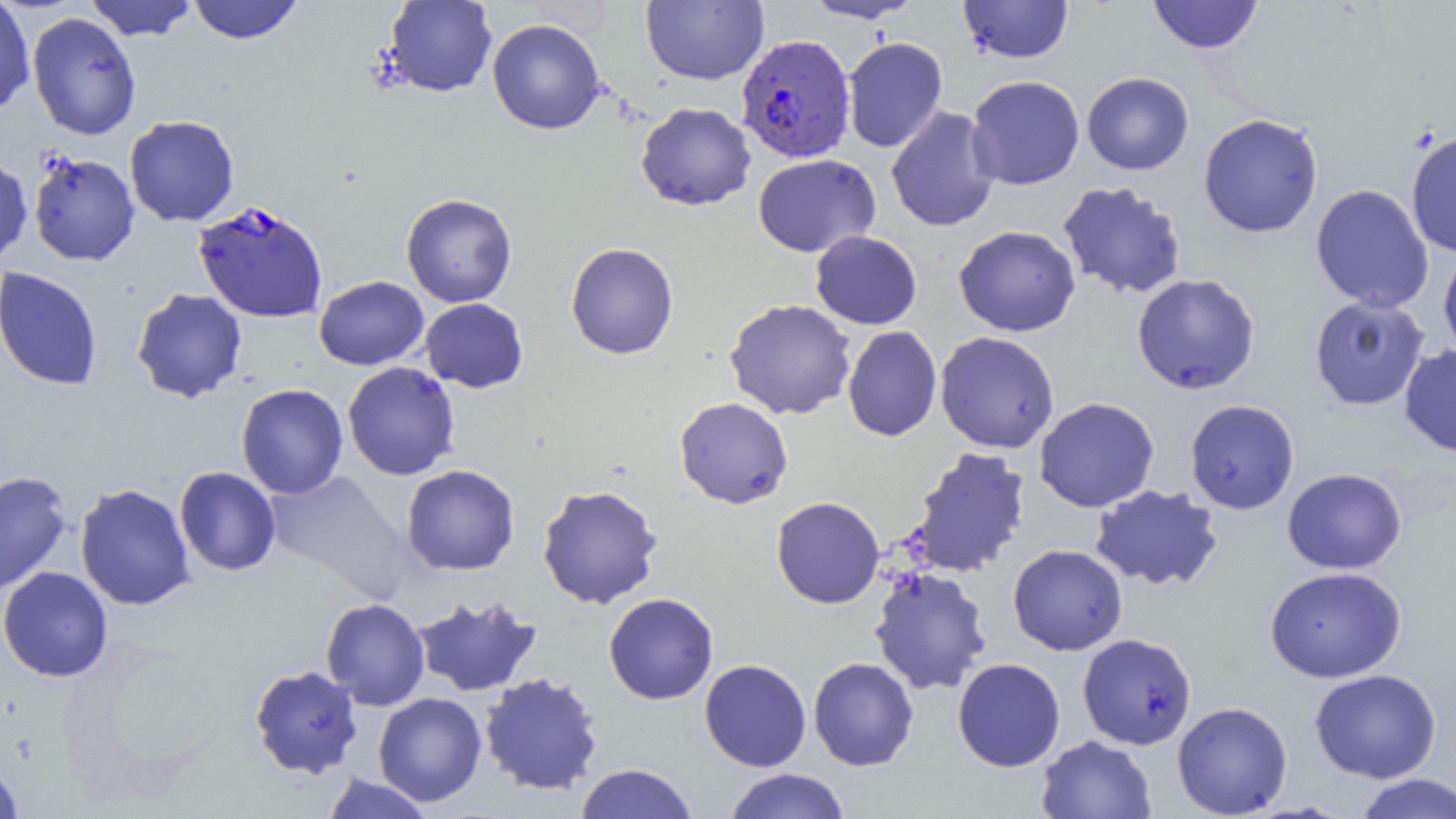

Approximate bounding boxes as named x1/y1/x2/y2 corners in pixels. Plasmodium falciparum-infected red blood cell locations: (x1=736, y1=34, x2=856, y2=163), (x1=193, y1=200, x2=328, y2=323). Uninfected red blood cell locations: (x1=0, y1=0, x2=35, y2=118), (x1=85, y1=0, x2=197, y2=41), (x1=187, y1=0, x2=304, y2=44), (x1=640, y1=0, x2=768, y2=85), (x1=802, y1=0, x2=923, y2=23), (x1=958, y1=0, x2=1074, y2=64), (x1=1147, y1=0, x2=1264, y2=54), (x1=382, y1=1, x2=498, y2=97), (x1=27, y1=11, x2=141, y2=140), (x1=487, y1=18, x2=605, y2=134), (x1=842, y1=37, x2=948, y2=153), (x1=1082, y1=72, x2=1194, y2=175), (x1=966, y1=75, x2=1084, y2=190), (x1=636, y1=101, x2=756, y2=211), (x1=886, y1=105, x2=1000, y2=232), (x1=1198, y1=113, x2=1324, y2=238), (x1=124, y1=115, x2=240, y2=227), (x1=1406, y1=130, x2=1456, y2=257), (x1=28, y1=151, x2=140, y2=266), (x1=0, y1=153, x2=33, y2=267), (x1=753, y1=154, x2=881, y2=257), (x1=1058, y1=181, x2=1186, y2=299), (x1=1311, y1=183, x2=1434, y2=313), (x1=401, y1=193, x2=517, y2=307), (x1=954, y1=225, x2=1080, y2=336), (x1=811, y1=230, x2=922, y2=330), (x1=565, y1=242, x2=678, y2=360), (x1=1438, y1=242, x2=1456, y2=360), (x1=0, y1=266, x2=102, y2=391), (x1=1132, y1=273, x2=1260, y2=394), (x1=314, y1=276, x2=428, y2=370), (x1=131, y1=288, x2=247, y2=403), (x1=1309, y1=295, x2=1430, y2=410), (x1=420, y1=298, x2=529, y2=393), (x1=724, y1=298, x2=856, y2=420), (x1=843, y1=326, x2=942, y2=441), (x1=935, y1=331, x2=1059, y2=453), (x1=1399, y1=345, x2=1456, y2=457), (x1=342, y1=362, x2=460, y2=480), (x1=236, y1=383, x2=348, y2=499), (x1=674, y1=396, x2=793, y2=509), (x1=1034, y1=397, x2=1160, y2=512), (x1=1185, y1=399, x2=1299, y2=514), (x1=909, y1=447, x2=1031, y2=577), (x1=401, y1=464, x2=520, y2=576), (x1=174, y1=467, x2=281, y2=576), (x1=1282, y1=468, x2=1407, y2=575), (x1=0, y1=470, x2=73, y2=594), (x1=265, y1=470, x2=412, y2=602), (x1=74, y1=483, x2=195, y2=611), (x1=537, y1=484, x2=663, y2=609), (x1=1089, y1=484, x2=1224, y2=592), (x1=771, y1=496, x2=885, y2=609), (x1=1008, y1=544, x2=1127, y2=656), (x1=0, y1=566, x2=113, y2=683), (x1=1264, y1=566, x2=1406, y2=682), (x1=869, y1=567, x2=992, y2=696), (x1=603, y1=593, x2=718, y2=704), (x1=412, y1=595, x2=541, y2=697), (x1=321, y1=598, x2=430, y2=710), (x1=1078, y1=633, x2=1196, y2=749), (x1=808, y1=657, x2=919, y2=771), (x1=952, y1=658, x2=1065, y2=772), (x1=699, y1=659, x2=811, y2=771), (x1=248, y1=664, x2=364, y2=780), (x1=1309, y1=668, x2=1441, y2=783), (x1=479, y1=672, x2=603, y2=796), (x1=373, y1=692, x2=487, y2=807), (x1=1172, y1=701, x2=1292, y2=818), (x1=1036, y1=734, x2=1156, y2=819), (x1=0, y1=761, x2=24, y2=818), (x1=575, y1=763, x2=699, y2=819), (x1=723, y1=768, x2=851, y2=819), (x1=321, y1=773, x2=435, y2=819), (x1=1355, y1=773, x2=1456, y2=819). Slide-level diagnosis: Plasmodium falciparum. Image is 1456×819 pixels. Captured at 1000x magnification. Optical microscopy. Thin blood smear. One field of a larger specimen.